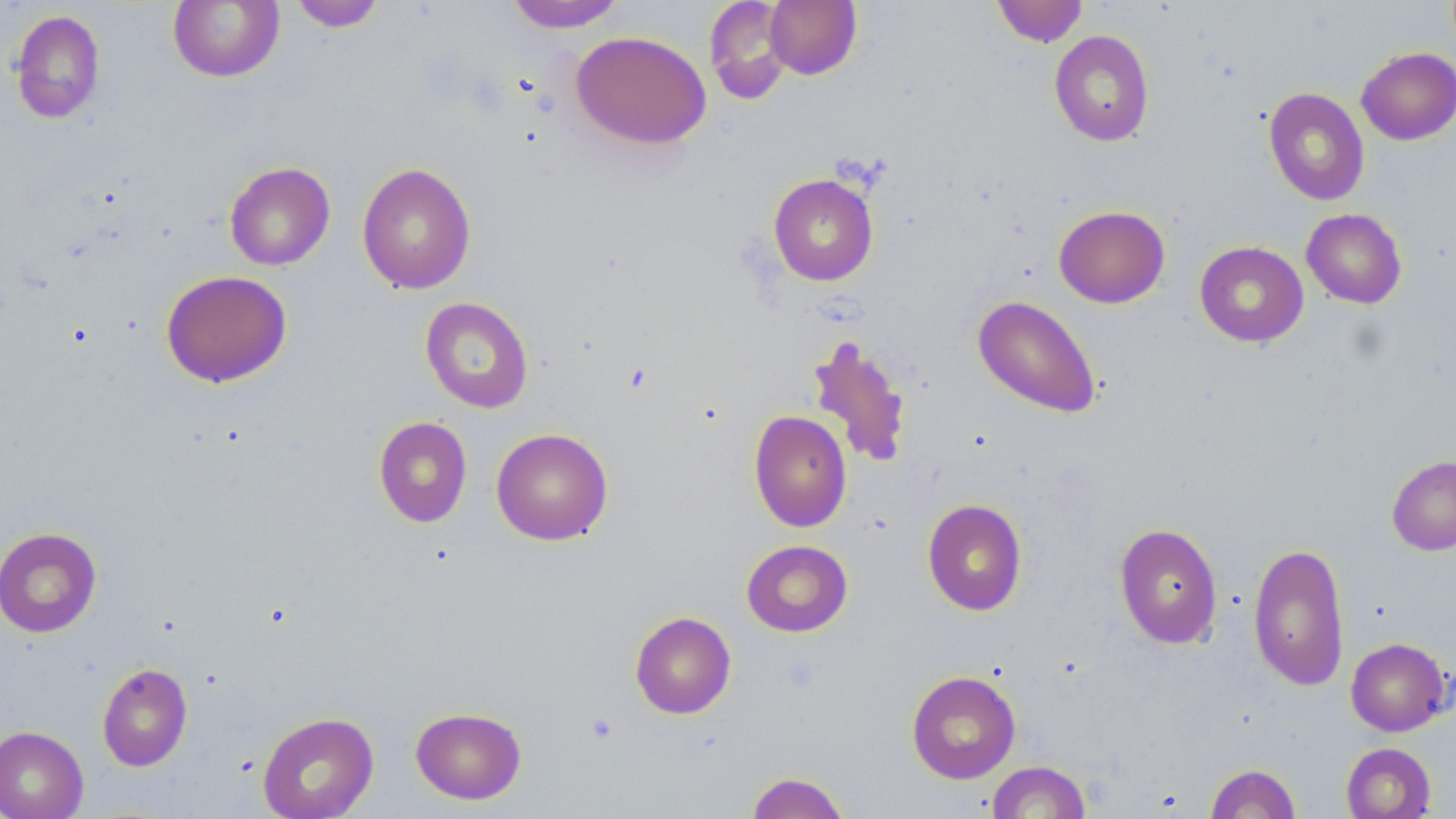

Summary:
  - Coordinate format: approximate bounding boxes as named x1/y1/x2/y2 corners in pixels
  - Uninfected red blood cell locations: (x1=289, y1=0, x2=386, y2=32), (x1=505, y1=0, x2=627, y2=32), (x1=764, y1=0, x2=861, y2=79), (x1=992, y1=0, x2=1088, y2=47), (x1=168, y1=1, x2=284, y2=82), (x1=704, y1=1, x2=795, y2=104), (x1=10, y1=9, x2=106, y2=123), (x1=570, y1=30, x2=711, y2=150), (x1=1049, y1=30, x2=1155, y2=146), (x1=1356, y1=47, x2=1456, y2=145), (x1=1263, y1=87, x2=1370, y2=206), (x1=224, y1=161, x2=335, y2=270), (x1=357, y1=163, x2=476, y2=295), (x1=768, y1=173, x2=879, y2=286), (x1=1053, y1=205, x2=1170, y2=308), (x1=1301, y1=208, x2=1407, y2=308), (x1=1194, y1=241, x2=1309, y2=347), (x1=161, y1=270, x2=292, y2=388), (x1=972, y1=295, x2=1102, y2=419), (x1=420, y1=297, x2=534, y2=413), (x1=805, y1=334, x2=913, y2=471), (x1=749, y1=409, x2=852, y2=532), (x1=373, y1=416, x2=472, y2=527), (x1=491, y1=427, x2=613, y2=545), (x1=1387, y1=455, x2=1456, y2=555), (x1=922, y1=498, x2=1027, y2=615), (x1=1114, y1=522, x2=1223, y2=649), (x1=0, y1=526, x2=102, y2=637), (x1=741, y1=539, x2=853, y2=637), (x1=1248, y1=541, x2=1349, y2=691), (x1=629, y1=611, x2=736, y2=719), (x1=1345, y1=637, x2=1451, y2=736), (x1=97, y1=662, x2=193, y2=771), (x1=906, y1=670, x2=1021, y2=783), (x1=410, y1=706, x2=527, y2=805), (x1=257, y1=711, x2=379, y2=818), (x1=0, y1=726, x2=89, y2=819), (x1=1341, y1=742, x2=1436, y2=819), (x1=986, y1=761, x2=1091, y2=818), (x1=1205, y1=763, x2=1301, y2=819), (x1=745, y1=771, x2=850, y2=819)
  - Platelet locations: (x1=585, y1=712, x2=619, y2=746)
  - Slide-level diagnosis: no evidence of blood parasites
  - Modality: optical microscopy
  - Stain: May-Grünwald-Giemsa
  - Magnification: 1000x
  - Image size: 1456×819 pixels
  - Preparation: thin blood film
  - Field of view: single